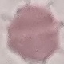

Summary:
  - Result: no malaria parasites detected
  - Capture: smartphone camera at the microscope eyepiece
  - Stain: Giemsa
  - Preparation: thin blood film
  - Image type: cell patch, automatically extracted from a larger field of view and resized to 64 × 64 pixels